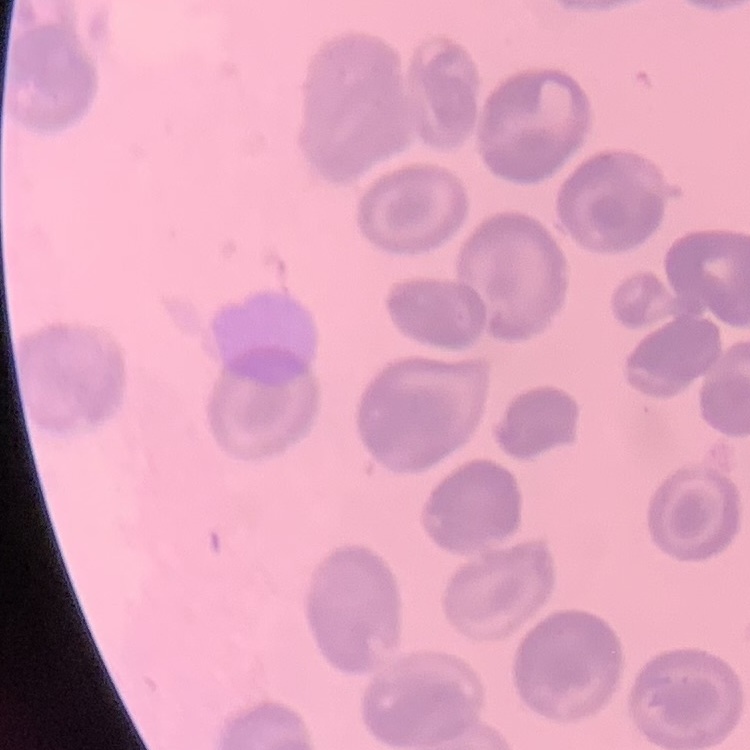
Summary:
  - Erythrocyte morphology: no rouleaux formation
  - Image type: square crop of a larger photomicrograph
  - Preparation: thin peripheral smear
  - Stain: Field's or Giemsa